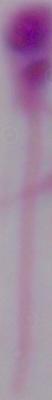

Summary:
  - Magnification: 1000x
  - Modality: photomicrograph
  - Identification: Leishmania